Classify this cell by malaria status.
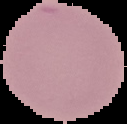

It is uninfected.

image type = cell region segmented out of the field of view; surrounding area masked to black
preparation = thin blood smear
image size = 127×124 pixels